Identify the parasite.
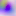

Toxoplasma gondii.

magnification = 400x
modality = photomicrograph